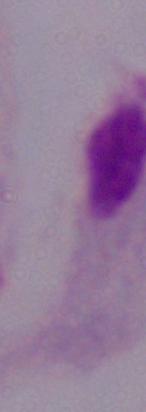
Photomicrograph. A trichomonad is seen. Captured at 1000x magnification.